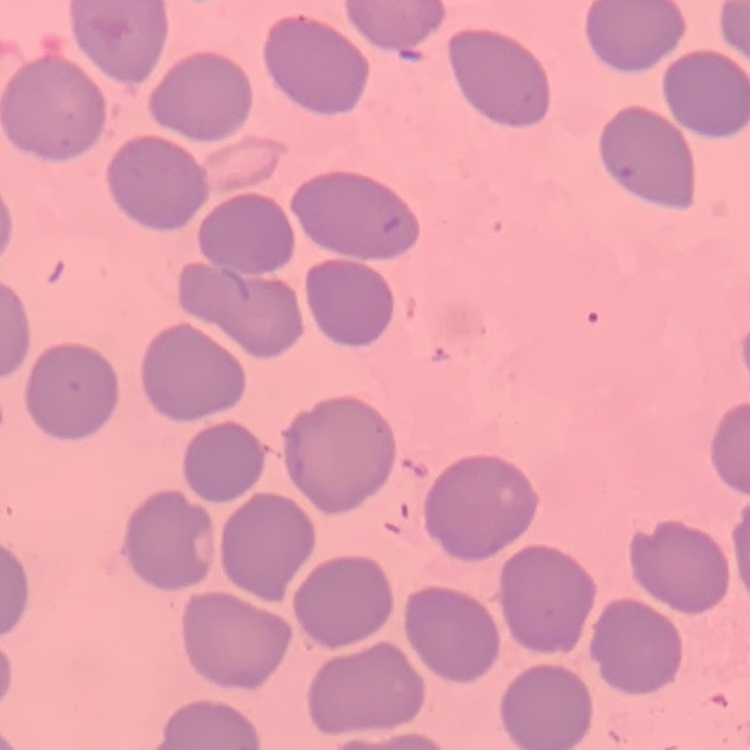

Summary:
  - Erythrocyte morphology: no rouleaux formation
  - Image type: square crop of a larger photomicrograph
  - Stain: Field's or Giemsa
  - Preparation: thin blood smear